Describe the morphology of the erythrocytes.
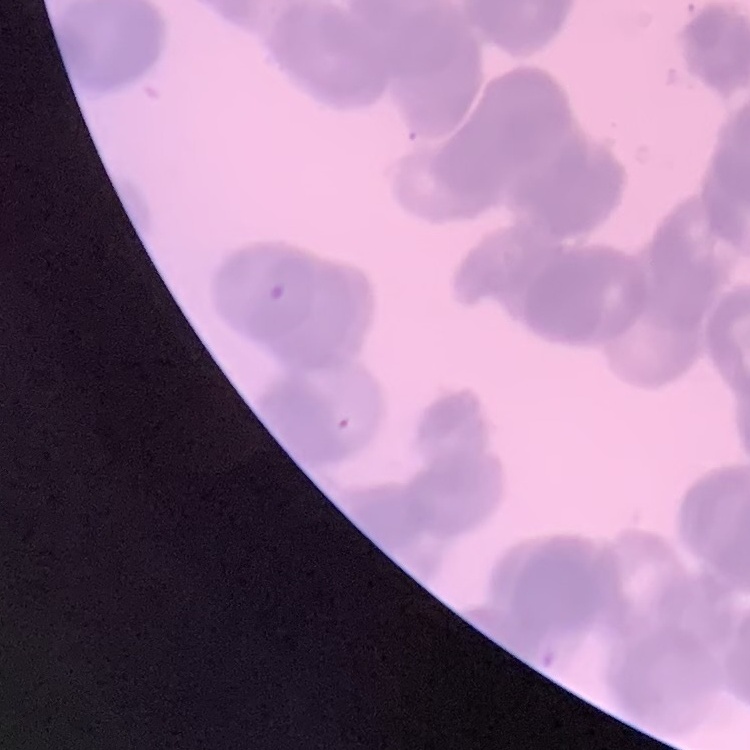
They show rouleaux formation.

One tile cut from a larger photomicrograph. Field's or Giemsa stain. Thin blood film.